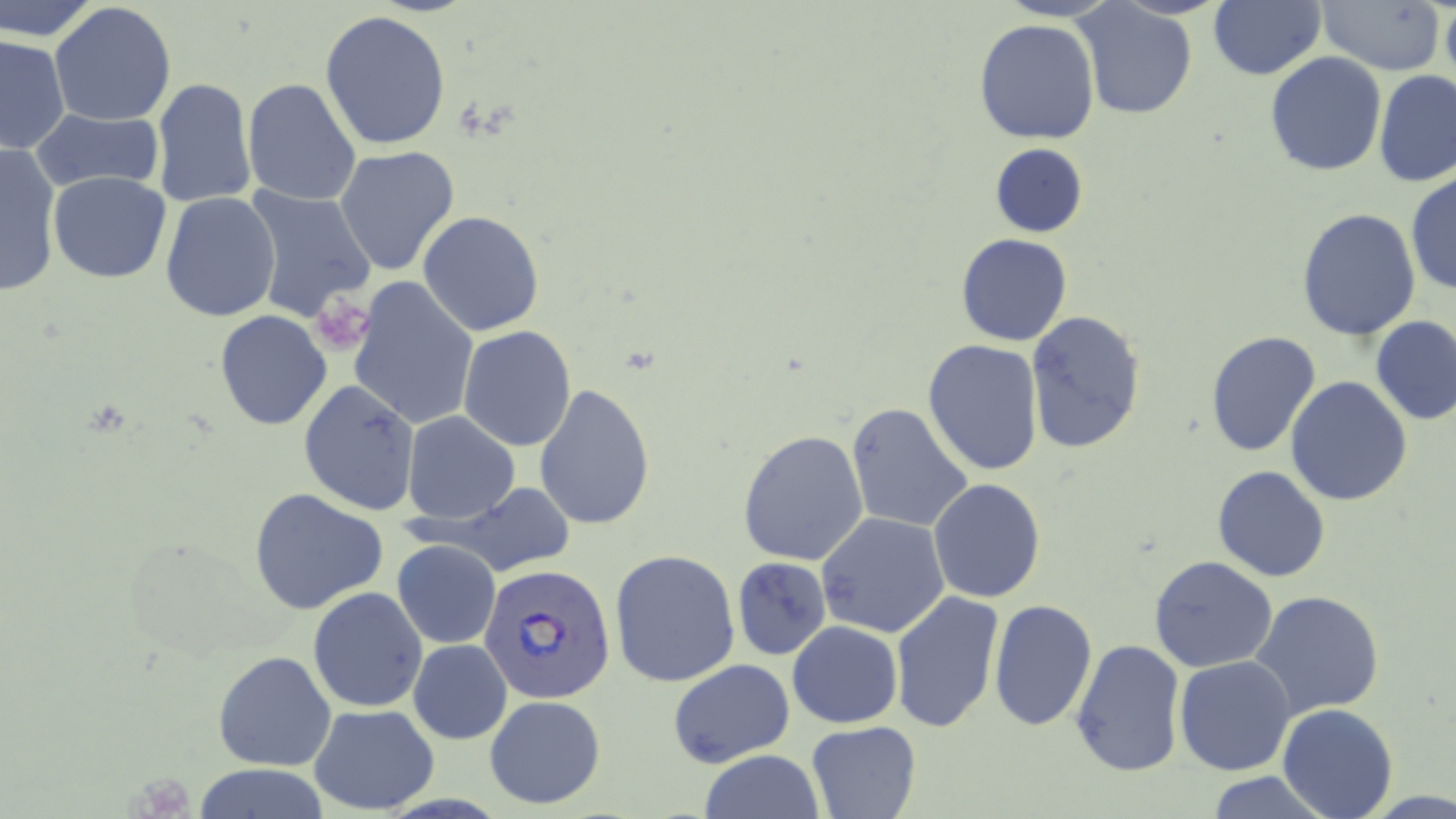
slide-level diagnosis = Plasmodium falciparum
modality = light microscopy
stain = May-Grünwald-Giemsa
image size = 1456×819 pixels
magnification = 1000x
platelet locations = approximate bounding boxes as (x1,y1)-(x2,y2) corner pairs in pixels: (311,294)-(371,356)
Plasmodium falciparum-infected red blood cell locations = approximate bounding boxes as (x1,y1)-(x2,y2) corner pairs in pixels: (480,562)-(615,706)
field of view = single
uninfected red blood cell locations = approximate bounding boxes as (x1,y1)-(x2,y2) corner pairs in pixels: (0,0)-(102,43), (998,0)-(1119,23), (1208,0)-(1325,81), (1315,0)-(1447,74), (1441,1)-(1456,89), (49,2)-(178,126), (1077,3)-(1199,119), (320,10)-(452,151), (974,19)-(1100,144), (1,35)-(70,154), (1263,51)-(1387,176), (1373,70)-(1456,188), (151,77)-(258,212), (240,77)-(362,206), (30,109)-(164,194), (1,142)-(64,299), (990,143)-(1089,237), (334,146)-(460,277), (47,170)-(173,285), (1407,174)-(1455,298), (243,185)-(379,325), (160,191)-(282,324), (1297,207)-(1420,341), (418,211)-(545,337), (955,233)-(1072,348), (348,276)-(479,431), (1025,311)-(1146,454), (214,312)-(332,430), (1371,316)-(1456,426), (458,326)-(576,449), (1205,331)-(1324,459), (921,339)-(1043,477), (1285,376)-(1414,507), (298,379)-(420,516), (533,383)-(656,530), (846,402)-(976,535), (403,411)-(520,524), (737,429)-(870,566), (1211,466)-(1330,582), (928,479)-(1045,603), (248,487)-(389,615), (447,488)-(573,574), (815,513)-(951,640), (393,540)-(501,650), (610,549)-(741,689), (1150,556)-(1278,673), (732,557)-(832,660), (308,586)-(427,713), (888,590)-(1004,734), (1252,591)-(1384,716), (989,599)-(1097,733), (787,620)-(902,729), (406,637)-(512,744), (1069,637)-(1185,778), (213,649)-(338,772), (1173,656)-(1297,775), (666,659)-(795,768), (484,694)-(607,811), (1277,702)-(1399,819), (308,704)-(439,813), (805,720)-(922,819), (698,750)-(825,819), (190,766)-(334,819), (1200,772)-(1334,818)
preparation = thin blood film